Evaluate for malaria.
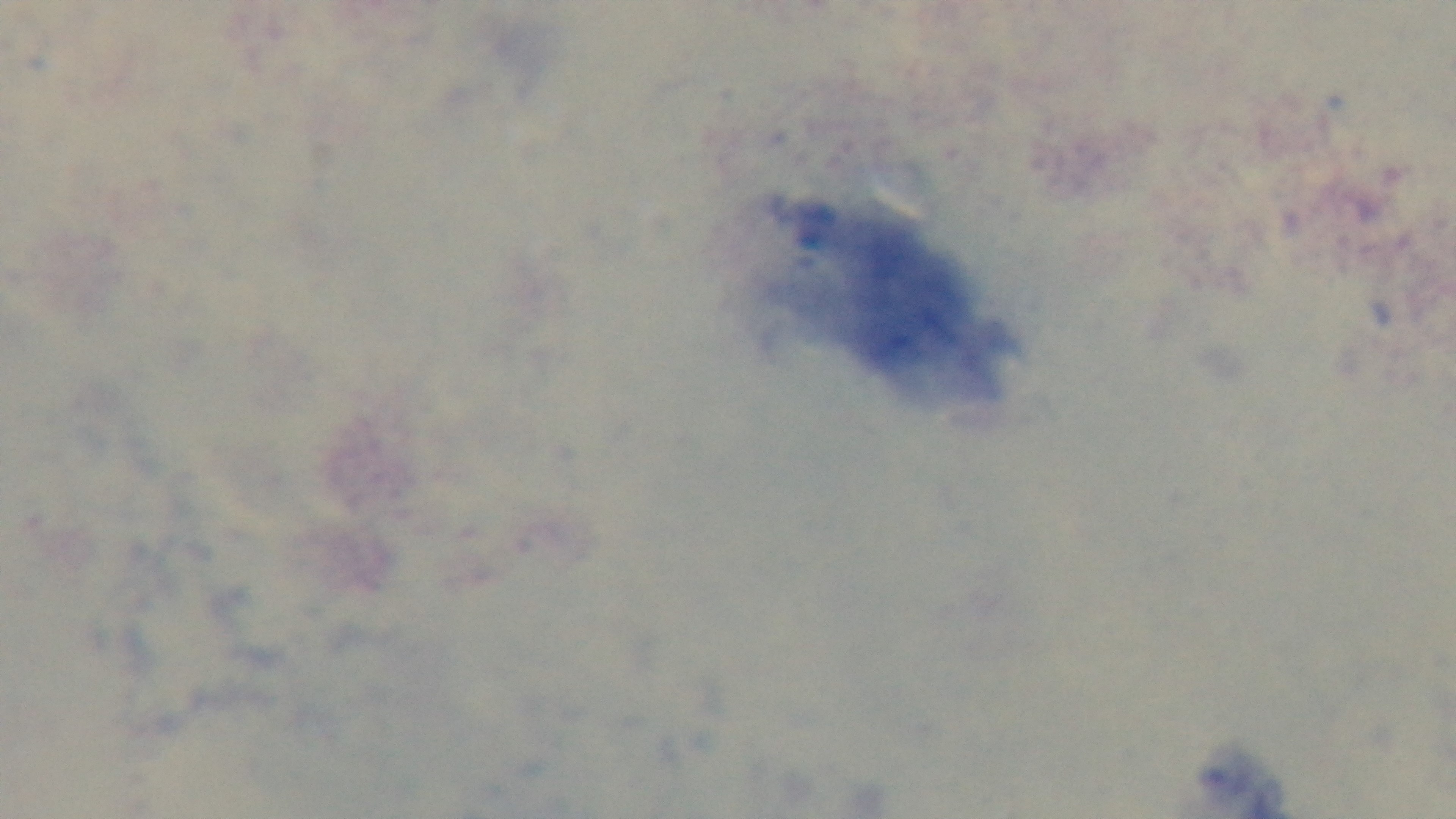

It is uninfected.

Summary:
  - Capture: mounted 4K digital camera
  - Stain: Giemsa
  - Objective: 100x oil immersion
  - Field of view: one from the slide
  - Preparation: thick smear
  - Modality: light microscopy